Name the cell type shown.
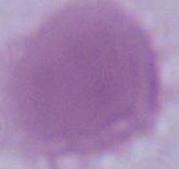
An erythrocyte.

1000x magnification. Micrograph.